Name the parasite shown.
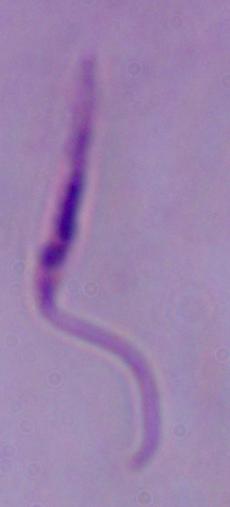
This is Leishmania.

Summary:
  - Modality: photomicrograph
  - Magnification: 1000x